Describe the morphology of the red blood cells.
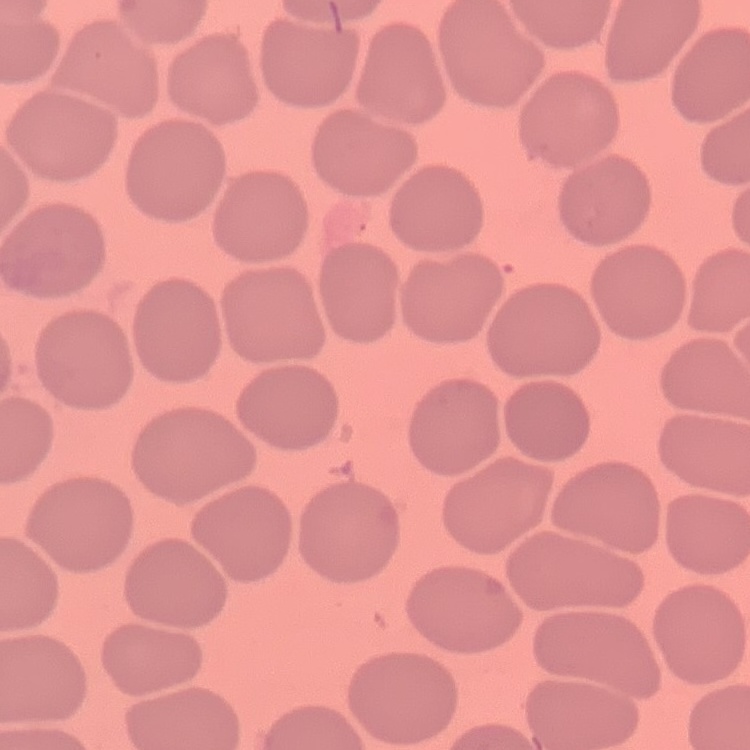
They show no rouleaux formation.

Thin blood film. Stained with either Field's or Giemsa. One tile cut from a larger photomicrograph.